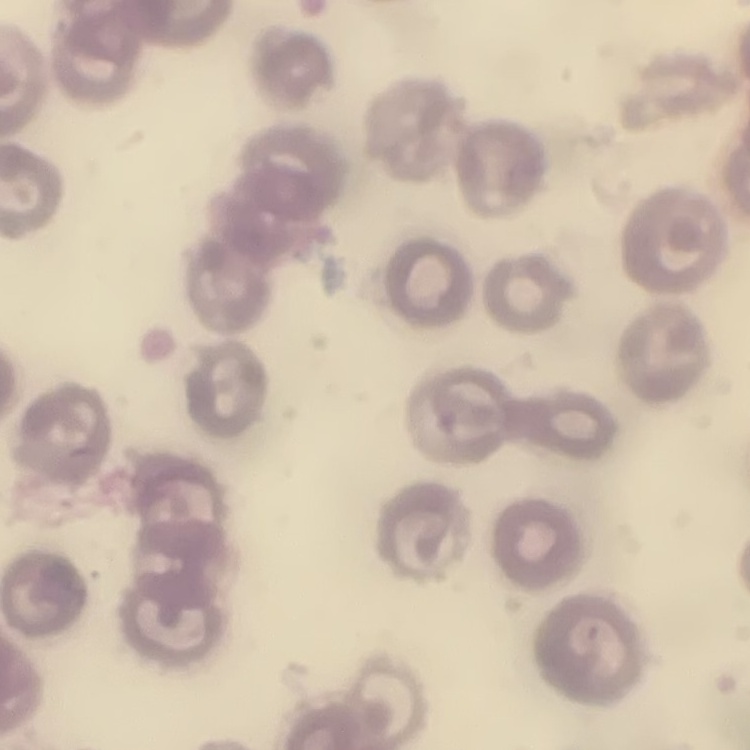

Summary:
  - Red blood cell morphology: no rouleaux formation
  - Image type: square crop of a larger photomicrograph
  - Stain: Field's or Giemsa
  - Preparation: thin peripheral smear